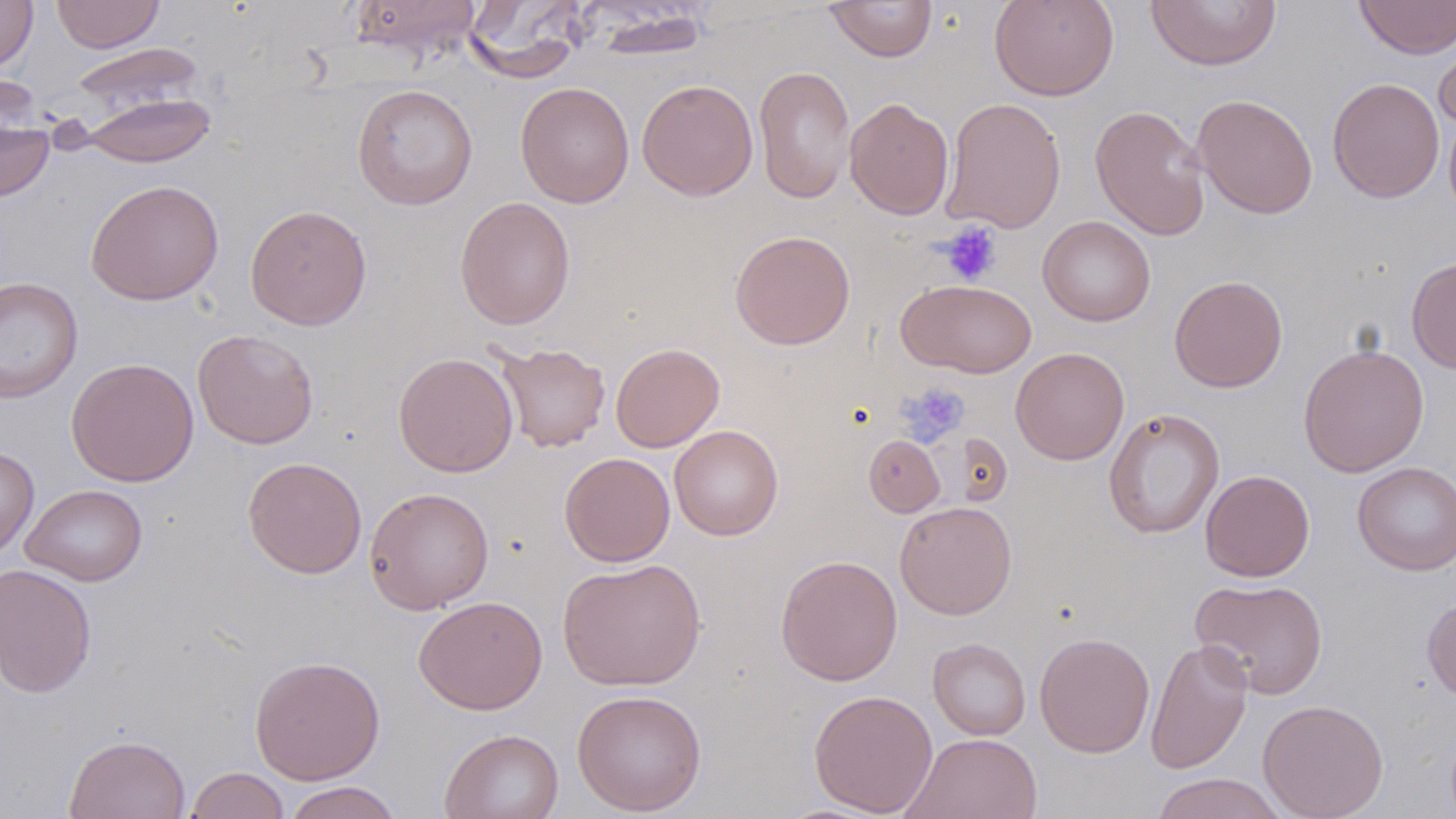
{
  "slide_level_diagnosis": "no evidence of blood parasites",
  "field_of_view": "one of a larger specimen",
  "preparation": "thin blood film",
  "magnification": "1000x",
  "stain": "May-Grünwald-Giemsa",
  "modality": "light microscopy",
  "uninfected_red_blood_cell_locations": "approximate bounding boxes as (x1, y1, x2, y2) in pixels: (0, 0, 38, 73), (51, 0, 164, 53), (348, 0, 483, 61), (460, 0, 588, 84), (989, 0, 1119, 101), (1146, 0, 1282, 70), (1354, 0, 1456, 59), (826, 1, 938, 62), (582, 6, 716, 59), (1435, 37, 1456, 137), (70, 42, 206, 116), (753, 65, 856, 204), (1327, 77, 1445, 203), (637, 79, 758, 200), (515, 81, 635, 208), (352, 83, 478, 210), (81, 92, 216, 167), (1192, 94, 1318, 218), (844, 97, 954, 219), (941, 97, 1067, 234), (1090, 104, 1211, 241), (0, 109, 54, 202), (85, 179, 224, 305), (454, 196, 576, 330), (245, 204, 372, 330), (1037, 215, 1156, 326), (729, 229, 855, 350), (1406, 257, 1456, 374), (1169, 275, 1288, 392), (0, 277, 83, 404), (897, 279, 1037, 378), (192, 329, 319, 449), (494, 342, 610, 452), (610, 342, 725, 452), (1298, 344, 1430, 477), (1010, 347, 1129, 465), (393, 351, 519, 477), (66, 357, 199, 487), (1103, 408, 1225, 539), (669, 425, 784, 541), (863, 435, 945, 516), (0, 445, 39, 560), (559, 452, 675, 567), (242, 457, 367, 579), (1352, 462, 1456, 575), (1200, 469, 1315, 582), (21, 484, 148, 586), (365, 486, 494, 614), (895, 501, 1017, 619), (775, 554, 903, 686), (557, 557, 706, 691), (0, 563, 97, 698), (1190, 577, 1329, 699), (413, 595, 548, 715), (1422, 596, 1456, 704), (1034, 631, 1155, 758), (928, 638, 1031, 740), (1144, 638, 1253, 774), (249, 655, 385, 785), (571, 689, 707, 816), (808, 689, 938, 817), (1257, 698, 1389, 819), (439, 729, 564, 819), (901, 732, 1043, 819), (64, 734, 191, 819), (185, 767, 289, 819), (1149, 772, 1288, 819), (282, 781, 403, 819)",
  "platelet_locations": "approximate bounding boxes as (x1, y1, x2, y2) in pixels: (938, 222, 1002, 285), (898, 381, 969, 445)",
  "image_size": "1456×819 pixels"
}